State which parasite is depicted.
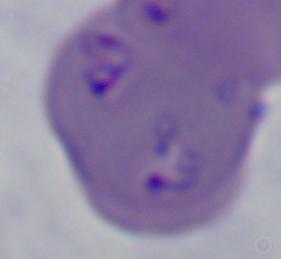
This is Babesia.

Summary:
  - Modality: micrograph
  - Magnification: 1000x